Outline each uninfected red blood cell.
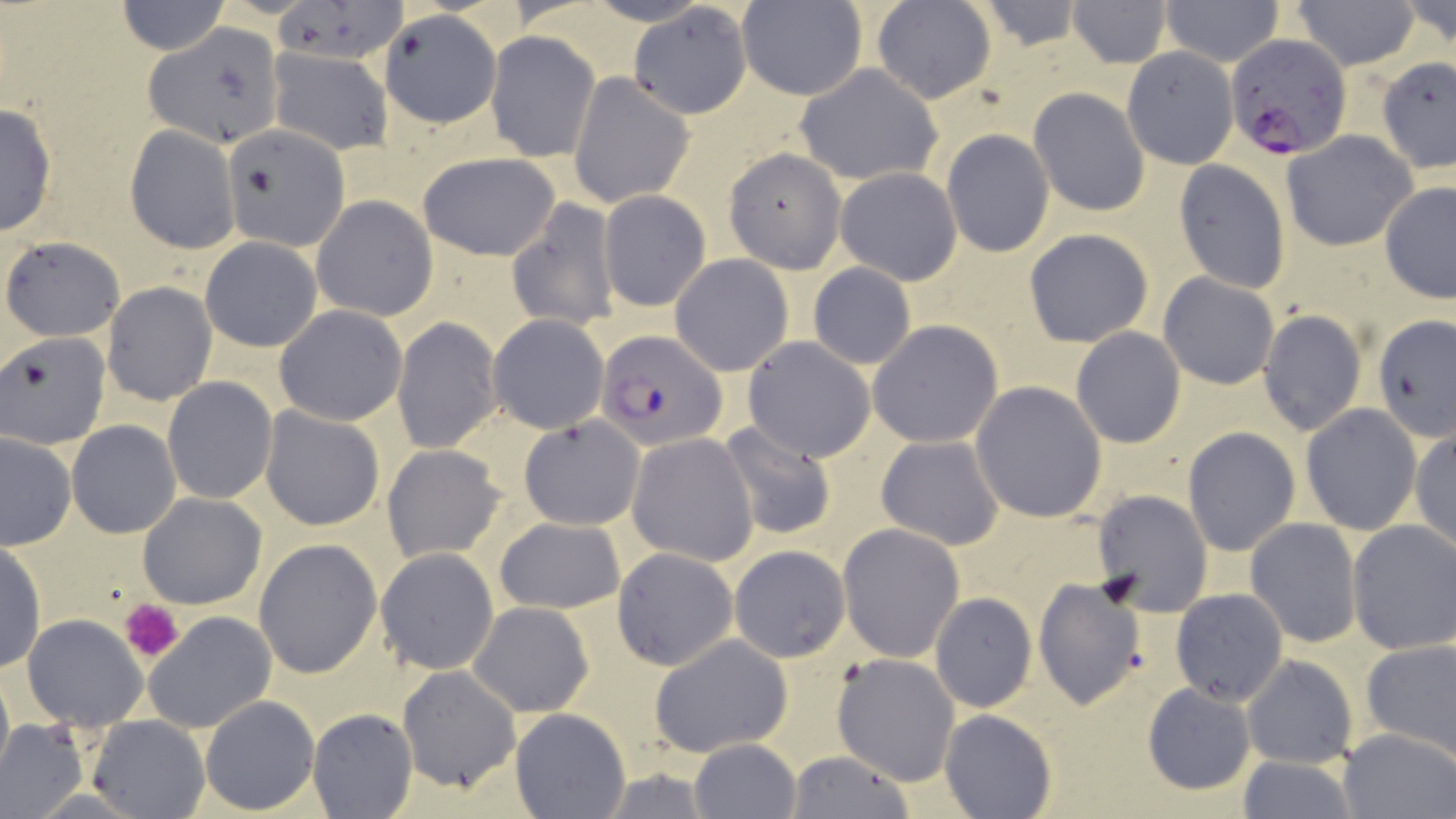
Approximate bounding boxes as [x1, y1, x2, y2] in pixels.
Uninfected red blood cells: [115, 0, 230, 54], [737, 0, 866, 99], [1291, 0, 1420, 70], [1393, 0, 1456, 49], [975, 1, 1086, 51], [1160, 1, 1284, 65], [871, 2, 996, 105], [1067, 2, 1172, 68], [277, 3, 407, 66], [627, 3, 754, 120], [381, 9, 502, 130], [146, 23, 286, 147], [485, 31, 600, 161], [267, 47, 392, 155], [1121, 47, 1238, 169], [1376, 55, 1456, 173], [793, 63, 945, 186], [571, 73, 694, 205], [1028, 87, 1149, 215], [0, 103, 57, 237], [224, 121, 350, 251], [123, 125, 240, 252], [941, 127, 1055, 258], [1281, 130, 1418, 250], [724, 148, 846, 274], [417, 152, 561, 261], [1173, 160, 1291, 293], [835, 168, 963, 285], [1379, 181, 1456, 303], [597, 191, 712, 312], [311, 195, 437, 321], [507, 197, 620, 332], [1023, 227, 1156, 348], [2, 236, 125, 344], [201, 236, 322, 352], [670, 254, 794, 376], [807, 263, 916, 370], [1157, 272, 1281, 390], [100, 281, 219, 406], [272, 304, 408, 425], [1256, 310, 1366, 433], [487, 314, 607, 433], [1374, 314, 1455, 445], [392, 317, 502, 454], [868, 321, 1002, 449], [1069, 327, 1186, 449], [0, 330, 113, 451], [742, 337, 875, 462], [162, 376, 279, 505], [971, 381, 1109, 523], [259, 404, 385, 531], [1299, 404, 1422, 536], [518, 415, 645, 531], [66, 420, 181, 539], [717, 420, 837, 540], [1183, 427, 1300, 556], [1411, 429, 1456, 555], [1, 433, 75, 551], [627, 433, 758, 566], [875, 435, 1006, 551], [381, 445, 506, 563], [1090, 489, 1214, 613], [138, 492, 267, 609], [494, 516, 628, 617], [1245, 518, 1362, 648], [1347, 522, 1456, 655], [837, 523, 965, 664], [253, 538, 383, 678], [0, 539, 47, 674], [728, 545, 851, 663], [375, 548, 499, 675], [612, 548, 738, 671], [1032, 574, 1150, 713], [1169, 589, 1287, 707], [929, 592, 1037, 712], [468, 601, 595, 717], [142, 610, 278, 735], [21, 613, 149, 733], [647, 632, 795, 757], [1360, 638, 1456, 763], [832, 655, 961, 786], [1241, 655, 1358, 768], [0, 664, 13, 783], [397, 665, 521, 794], [1141, 682, 1258, 798], [198, 695, 321, 816], [307, 708, 418, 818], [509, 708, 631, 818], [940, 709, 1056, 818], [85, 714, 210, 819], [1, 723, 87, 818], [1337, 728, 1454, 819], [688, 738, 801, 819], [784, 751, 917, 819], [1235, 757, 1358, 818].

Platelet locations: [121, 599, 182, 661]. Plasmodium falciparum-infected red blood cell locations: [1225, 34, 1353, 160], [597, 329, 725, 450]. Slide-level diagnosis: Plasmodium falciparum. Thin blood film. Captured at 1000x magnification. One field of a larger specimen. Light microscopy. May-Grünwald-Giemsa-stained preparation. Image is 1456×819 pixels.